Identify the preparation type.
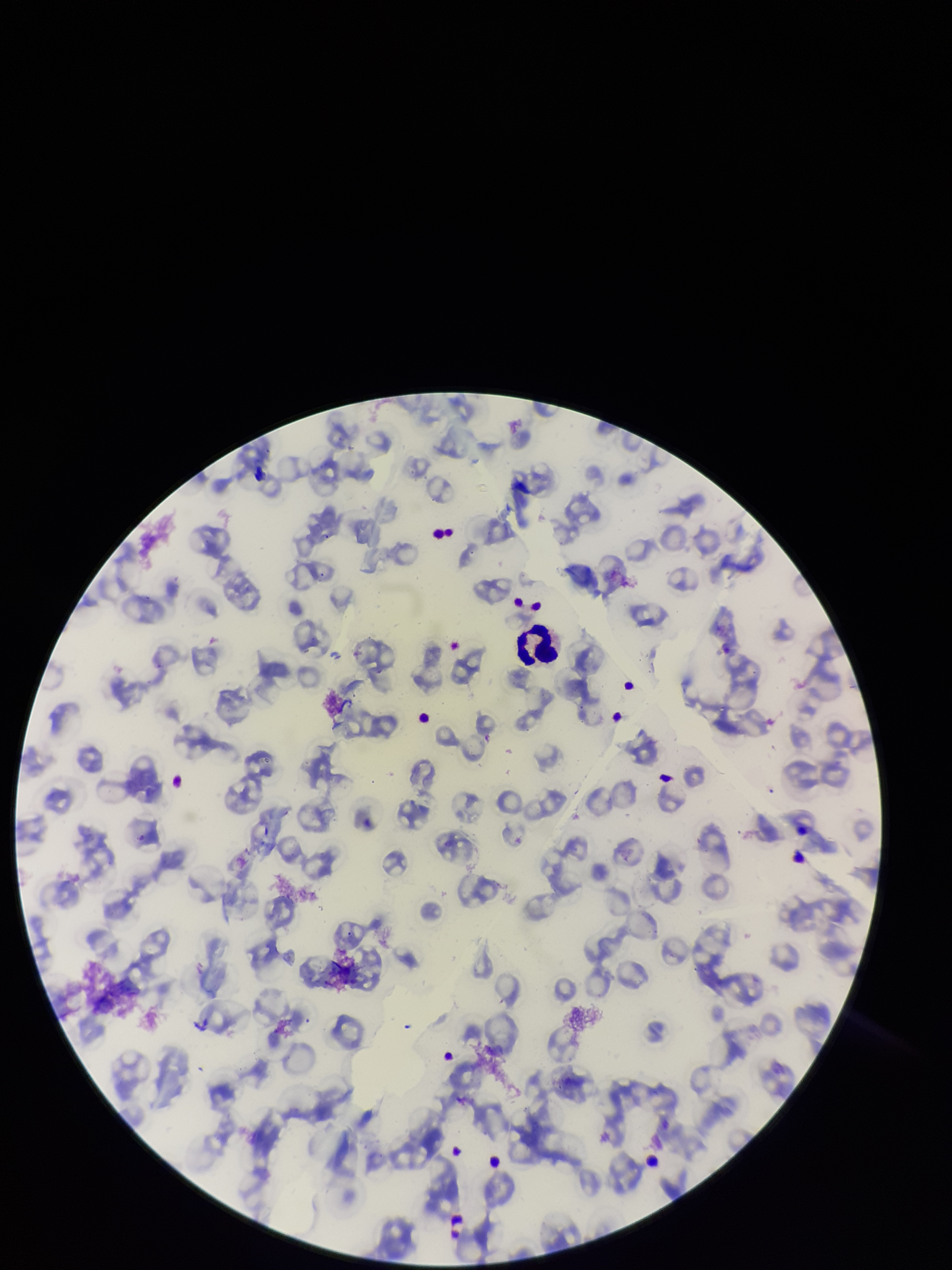

A thin smear.

Summary:
  - Parasitized red blood cells: none identified
  - Parasitized red blood cell count: 0
  - Image size: 952×1270 pixels
  - Field of view: single
  - Capture: smartphone photograph through the microscope eyepiece
  - Red blood cell count: 125
  - Species reported for this patient: Plasmodium falciparum
  - Patient malaria status: positive
  - Stain: Giemsa